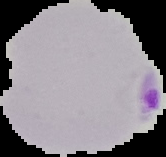
malaria_status: parasitized
image_type: segmented cell region on a black background
image_size: 166×157 pixels
preparation: thin blood film